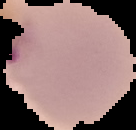
Result: malaria parasites detected. Cell region segmented out of the field of view; the surrounding area is masked to black. From a thin blood smear. Image is 136×130 pixels.